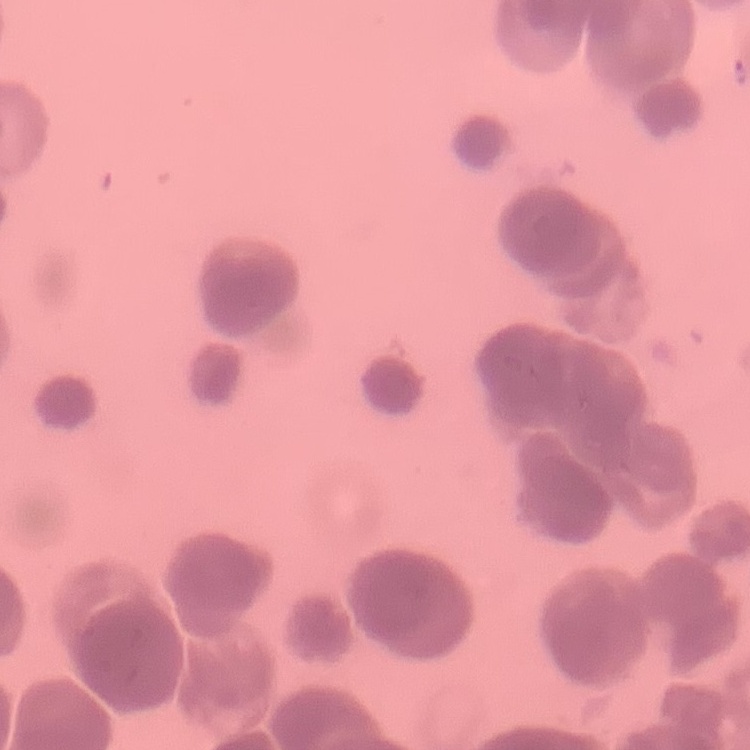 The red blood cells exhibit rouleaux formation. Thin blood film. Square crop of a larger photomicrograph. Field's or Giemsa stain.